Describe the morphology of the erythrocytes.
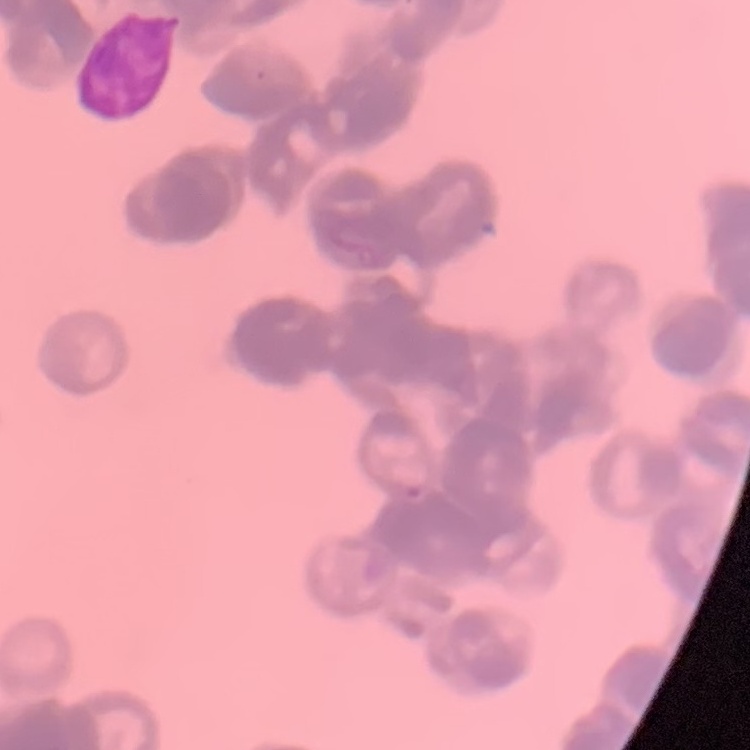
They show rouleaux formation.

Stained with either Field's or Giemsa. Thin blood film. Square crop of a larger photomicrograph.